Describe the morphology of the erythrocytes.
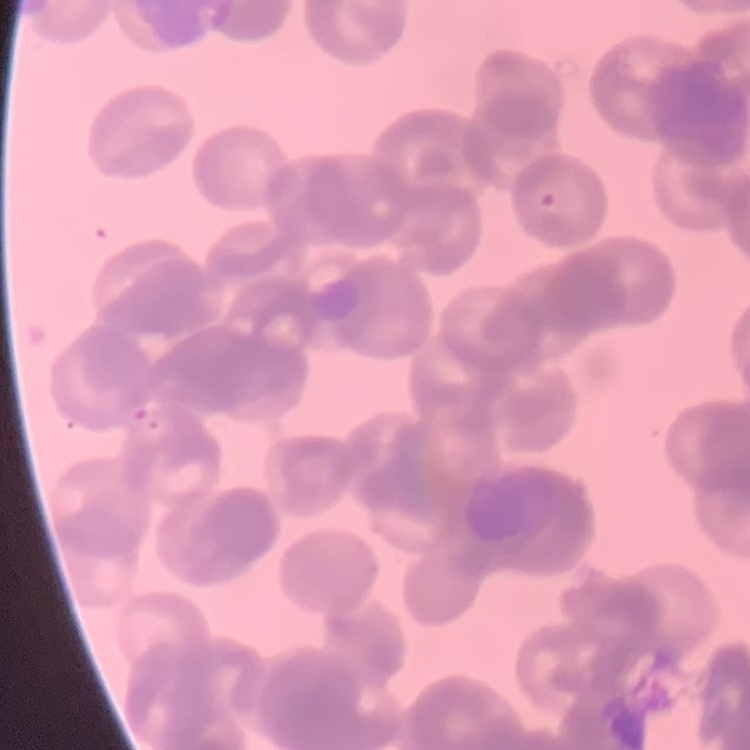
They show rouleaux formation.

Thin blood film. One tile cut from a larger photomicrograph. Stained with either Field's or Giemsa.